Outline each blood parasite and name the species.
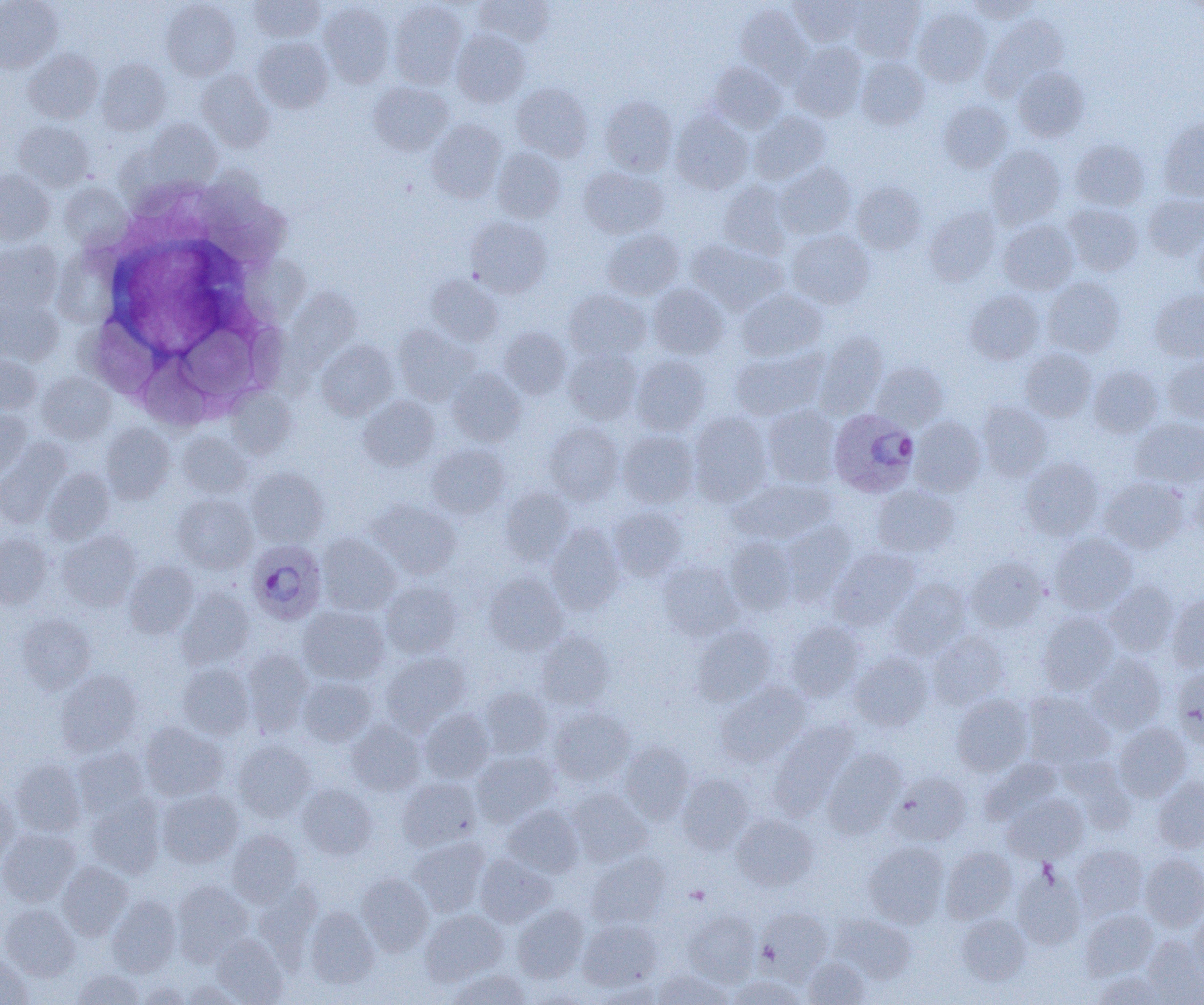

Approximate bounding boxes as [x1, y1, x2, y2] in pixels.
Plasmodium ovale-infected red blood cells: [828, 409, 918, 497], [246, 540, 327, 625].
No Plasmodium falciparum, Plasmodium malariae, Plasmodium vivax, Babesia divergens, or Trypanosoma brucei observed.

slide-level diagnosis = Plasmodium ovale
uninfected red blood cell locations = approximate bounding boxes as [x1, y1, x2, y2] in pixels: [248, 0, 326, 42], [789, 0, 865, 47], [849, 0, 925, 62], [967, 0, 1040, 23], [0, 1, 62, 73], [161, 1, 241, 80], [388, 1, 467, 88], [475, 1, 555, 46], [318, 2, 394, 88], [735, 3, 812, 83], [912, 6, 991, 87], [983, 15, 1068, 98], [452, 28, 530, 107], [253, 37, 333, 113], [790, 42, 867, 121], [23, 49, 103, 124], [857, 56, 929, 129], [97, 58, 170, 135], [708, 62, 786, 133], [1013, 66, 1089, 142], [196, 70, 274, 151], [369, 82, 453, 156], [511, 83, 593, 160], [600, 95, 677, 176], [938, 100, 1012, 173], [670, 110, 754, 194], [749, 111, 830, 184], [1158, 119, 1204, 201], [13, 120, 94, 190], [145, 120, 222, 190], [427, 120, 506, 202], [1070, 139, 1149, 211], [986, 145, 1066, 227], [493, 147, 566, 223], [775, 163, 856, 239], [578, 166, 668, 238], [0, 169, 55, 244], [717, 181, 792, 259], [852, 182, 925, 254], [59, 183, 130, 250], [1143, 194, 1204, 261], [1063, 203, 1144, 276], [925, 206, 1001, 285], [466, 217, 552, 297], [998, 220, 1078, 295], [602, 228, 684, 300], [1192, 229, 1204, 301], [786, 230, 874, 309], [687, 238, 786, 314], [0, 240, 63, 313], [426, 275, 503, 346], [1042, 277, 1125, 357], [649, 284, 729, 359], [563, 288, 651, 361], [737, 288, 827, 361], [1149, 289, 1204, 363], [966, 290, 1044, 364], [0, 299, 63, 365], [393, 325, 479, 405], [499, 327, 572, 398], [816, 331, 888, 417], [316, 340, 397, 420], [563, 347, 642, 424], [1020, 347, 1097, 422], [730, 348, 826, 421], [631, 354, 711, 435], [0, 355, 41, 416], [1163, 357, 1204, 426], [871, 362, 948, 431], [1088, 365, 1162, 438], [448, 369, 527, 446], [36, 372, 116, 444], [225, 387, 296, 459], [359, 395, 440, 470], [977, 401, 1052, 480], [761, 405, 840, 487], [0, 410, 33, 477], [689, 412, 772, 504], [910, 417, 986, 496], [1131, 418, 1204, 488], [544, 422, 624, 505], [100, 424, 174, 504], [618, 430, 699, 508], [178, 432, 252, 498], [0, 440, 71, 528], [427, 443, 510, 518], [1020, 458, 1103, 540], [245, 467, 328, 547], [43, 468, 114, 544], [1191, 471, 1204, 538], [1100, 477, 1189, 553], [730, 478, 835, 544], [872, 485, 960, 557], [500, 486, 574, 565], [173, 493, 257, 573], [370, 500, 461, 579], [610, 506, 686, 581], [781, 521, 857, 600], [547, 524, 624, 613], [57, 530, 140, 612], [1049, 532, 1137, 614], [0, 533, 52, 609], [317, 533, 400, 615], [724, 537, 797, 615], [829, 547, 918, 629], [966, 557, 1048, 632], [659, 560, 742, 640], [124, 562, 198, 638], [483, 573, 568, 655], [890, 579, 971, 658], [380, 581, 462, 658], [1104, 581, 1179, 657], [176, 588, 254, 669], [1167, 594, 1204, 672], [299, 606, 390, 685], [1037, 611, 1118, 694], [16, 613, 96, 693], [786, 620, 866, 701], [693, 625, 775, 706], [535, 630, 614, 709], [928, 632, 1008, 709], [242, 649, 313, 736], [380, 652, 470, 732], [850, 652, 932, 730], [1086, 653, 1167, 733], [176, 663, 254, 739], [1171, 667, 1204, 749], [56, 670, 143, 756], [298, 676, 377, 747], [716, 682, 809, 766], [479, 686, 553, 758], [1023, 692, 1114, 770], [952, 694, 1033, 776], [549, 707, 634, 785], [420, 709, 494, 782], [346, 720, 427, 796], [771, 720, 858, 815], [138, 721, 227, 801], [1114, 723, 1191, 801], [232, 740, 316, 821], [620, 742, 694, 823], [72, 746, 149, 818], [823, 749, 906, 837], [472, 750, 559, 826], [1059, 755, 1136, 832], [979, 757, 1062, 825], [9, 759, 84, 836], [888, 772, 970, 846], [677, 773, 754, 853], [397, 777, 481, 850], [1153, 778, 1204, 852], [297, 783, 377, 859], [157, 789, 243, 867], [568, 789, 652, 866], [0, 790, 18, 867], [87, 794, 165, 878], [1002, 794, 1088, 864], [503, 805, 584, 877], [732, 814, 818, 891], [0, 828, 80, 906], [227, 830, 303, 906], [408, 837, 489, 915], [864, 841, 949, 927], [1072, 844, 1147, 919], [940, 847, 1017, 923], [586, 853, 670, 929], [1139, 853, 1204, 932], [475, 854, 557, 927], [57, 861, 133, 940], [1012, 870, 1085, 951], [357, 873, 433, 955], [172, 881, 254, 965], [252, 881, 322, 966], [107, 895, 181, 977], [1, 904, 79, 980], [513, 905, 589, 982], [304, 906, 379, 988], [757, 909, 833, 980], [1080, 909, 1158, 979], [1189, 909, 1204, 983], [420, 910, 508, 985], [682, 910, 760, 986], [831, 914, 916, 983], [957, 915, 1030, 985], [578, 918, 662, 990], [211, 934, 288, 1004], [1141, 937, 1204, 1003], [0, 955, 33, 1005], [804, 957, 869, 1005], [72, 968, 144, 1004], [448, 968, 531, 1004], [654, 969, 731, 1005], [1091, 970, 1166, 1005], [727, 975, 807, 1005], [180, 979, 244, 1005], [592, 980, 664, 1005], [135, 982, 191, 1005]
modality = light microscopy
image size = 1204×1005 pixels
field of view = one of a larger specimen
preparation = thin blood film
magnification = 1000x